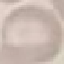
Malaria status: uninfected. Giemsa stain. Photographed with a smartphone camera at the microscope eyepiece. Automatically extracted cell patch, resized to 64 × 64 pixels. Thin blood smear.